State which parasite is depicted.
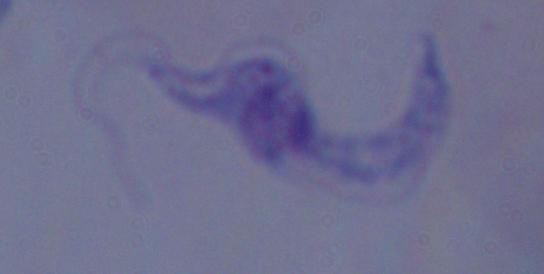

A trypanosome.

Summary:
  - Magnification: 1000x
  - Modality: photomicrograph